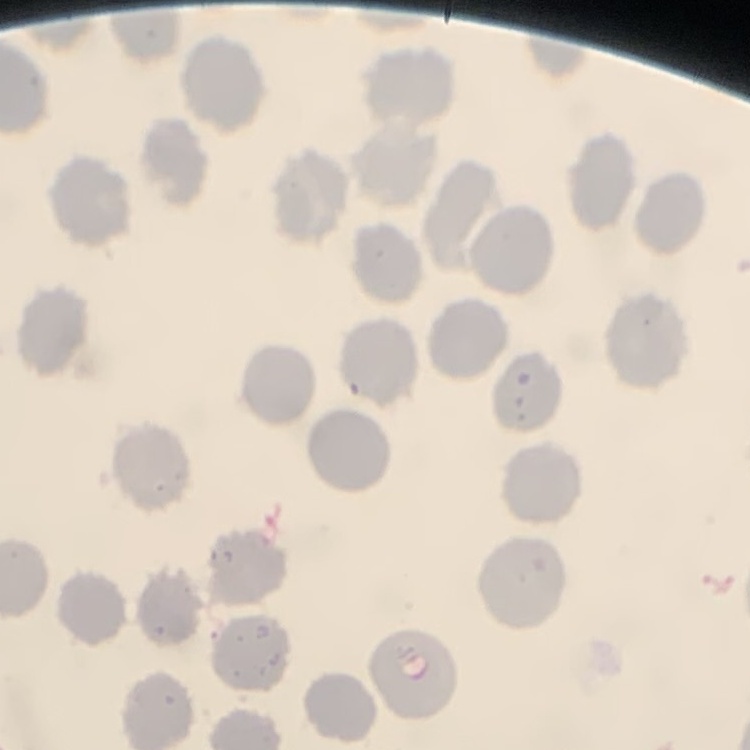

red_blood_cell_morphology: no rouleaux formation
image_type: one tile cut from a larger photomicrograph
preparation: thin peripheral smear
stain: Field's or Giemsa